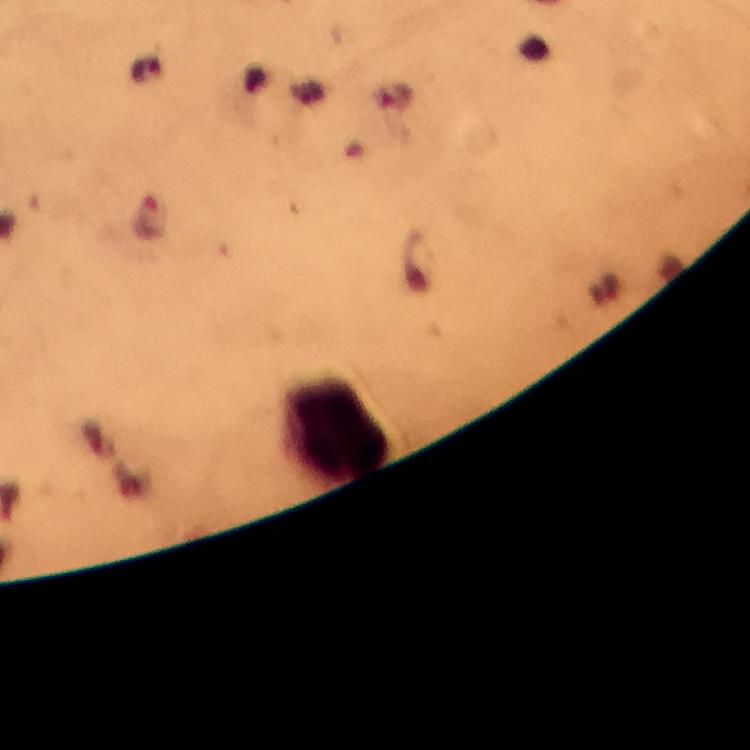

Approximate centers as [x, y] in pixels. Leukocyte locations: [337, 428]. From a malaria diagnostic workup. Plasmodium parasites: none detected. At 100x magnification. Immersion oil was used. Cropped region of a single field of view. Photographed through the microscope with a smartphone camera. Image is 750×750 pixels. Thick blood film. Giemsa stain.